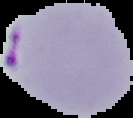
Summary:
  - Image size: 133×118 pixels
  - Result: malaria parasites identified
  - Preparation: thin blood smear
  - Image type: cell region segmented out of the field of view; surrounding area masked to black